Classify this cell by malaria status.
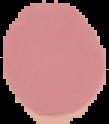

Uninfected.

preparation = thin blood smear
image type = segmented cell region with the area outside set to black
image size = 109×124 pixels